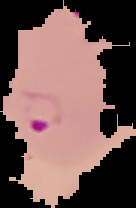
Summary:
  - Preparation: thin blood film
  - Image size: 136×208 pixels
  - Image type: cell region segmented out of the field of view; surrounding area masked to black
  - Result: malaria parasites detected